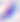
Captured at 400x magnification. Toxoplasma gondii is seen. Photomicrograph.